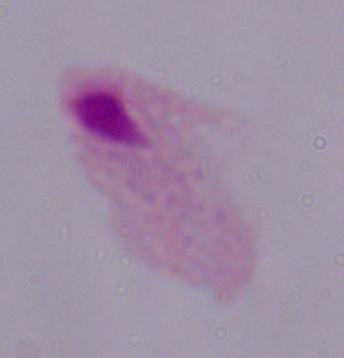

A trichomonad is seen. Captured at 1000x magnification. Micrograph.